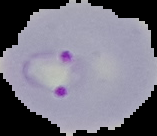
Malaria status: parasitized. The area outside the segmented cell region is set to black. Image is 157×136 pixels. From a thin blood film.